Name the cell type shown.
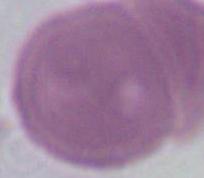
This is an erythrocyte.

{
  "magnification": "1000x",
  "modality": "micrograph"
}